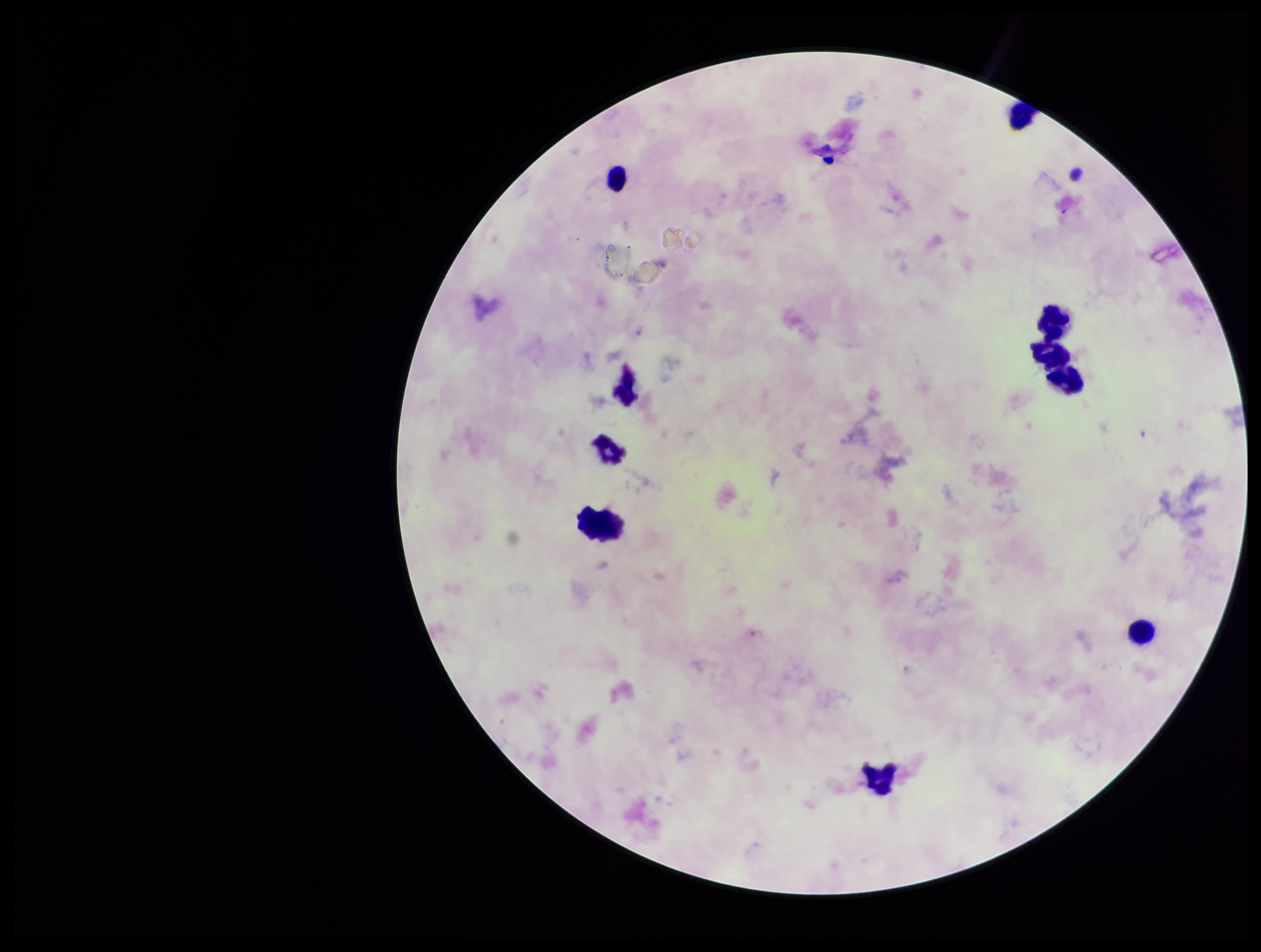
Summary:
  - Preparation: thick blood smear
  - Patient malaria status: infected
  - Image size: 1261×952 pixels
  - Capture: smartphone photograph through the microscope eyepiece
  - Leukocyte count: 9
  - Parasite count: 0
  - Field of view: single
  - Stain: Giemsa
  - Species reported for this patient: Plasmodium falciparum
  - Plasmodium parasites: none seen